Comment on the morphology of the erythrocytes.
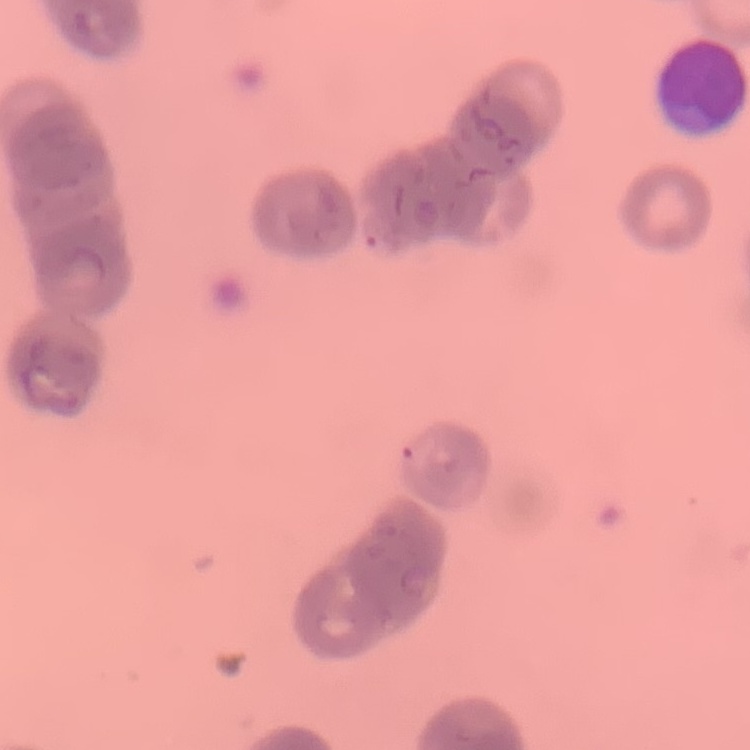

Rouleaux formation.

Summary:
  - Stain: Field's or Giemsa
  - Image type: one tile cut from a larger photomicrograph
  - Preparation: thin blood film